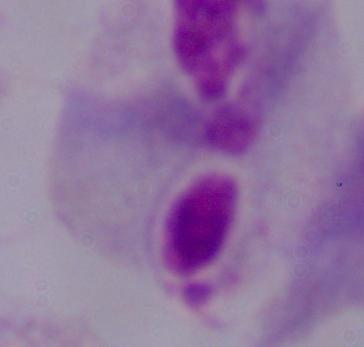 Photomicrograph. 1000x magnification. A trichomonad is seen.